Evaluate for Plasmodium parasites.
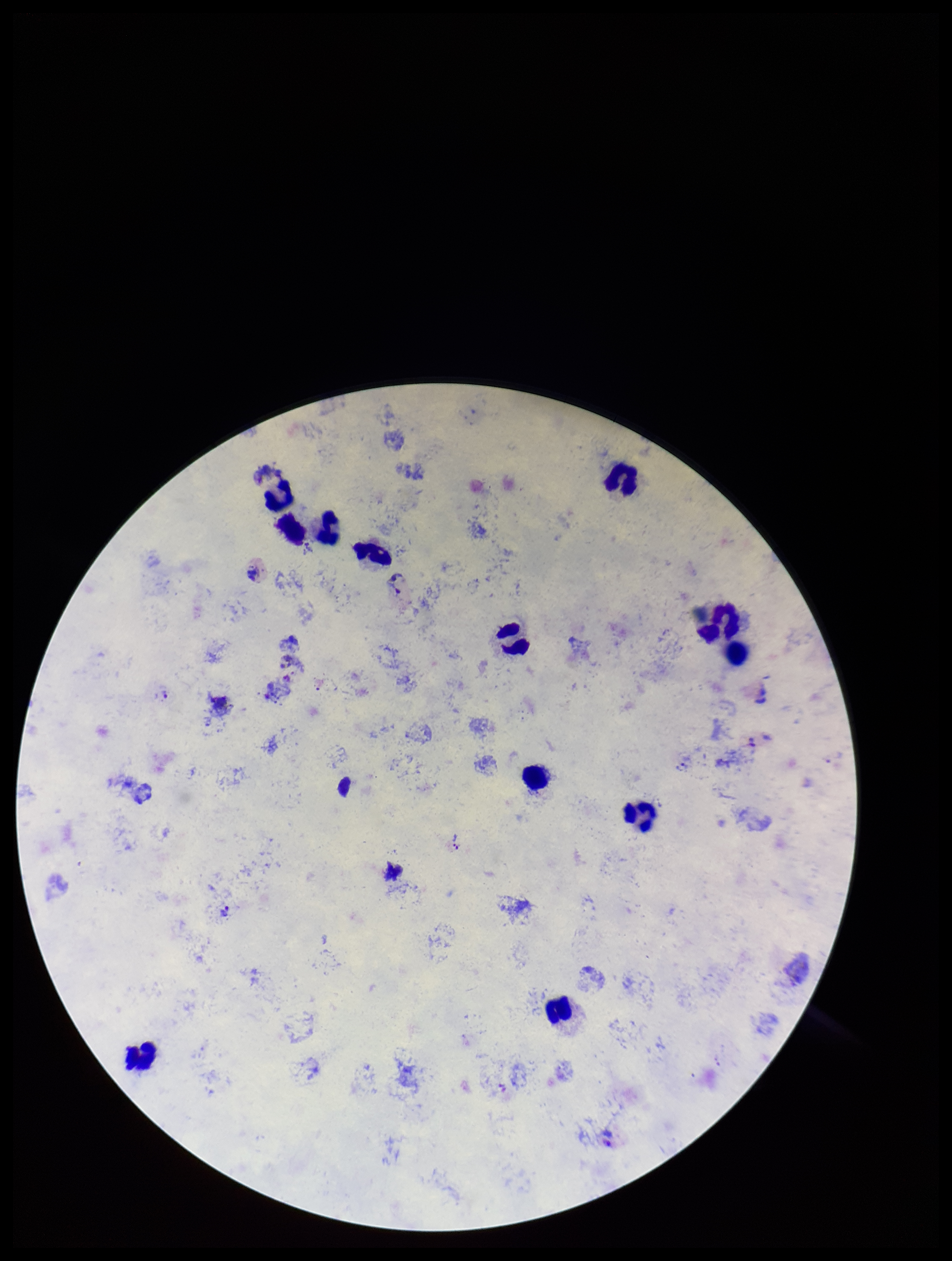

Identified.

capture = smartphone photograph through the microscope eyepiece
leukocyte count = 12
field of view = one from this slide
preparation = thick blood smear
stain = Giemsa
parasite count = 2
species reported for this patient = Plasmodium vivax
patient malaria status = infected
image size = 952×1261 pixels